Outline each Plasmodium ovale-infected red blood cell.
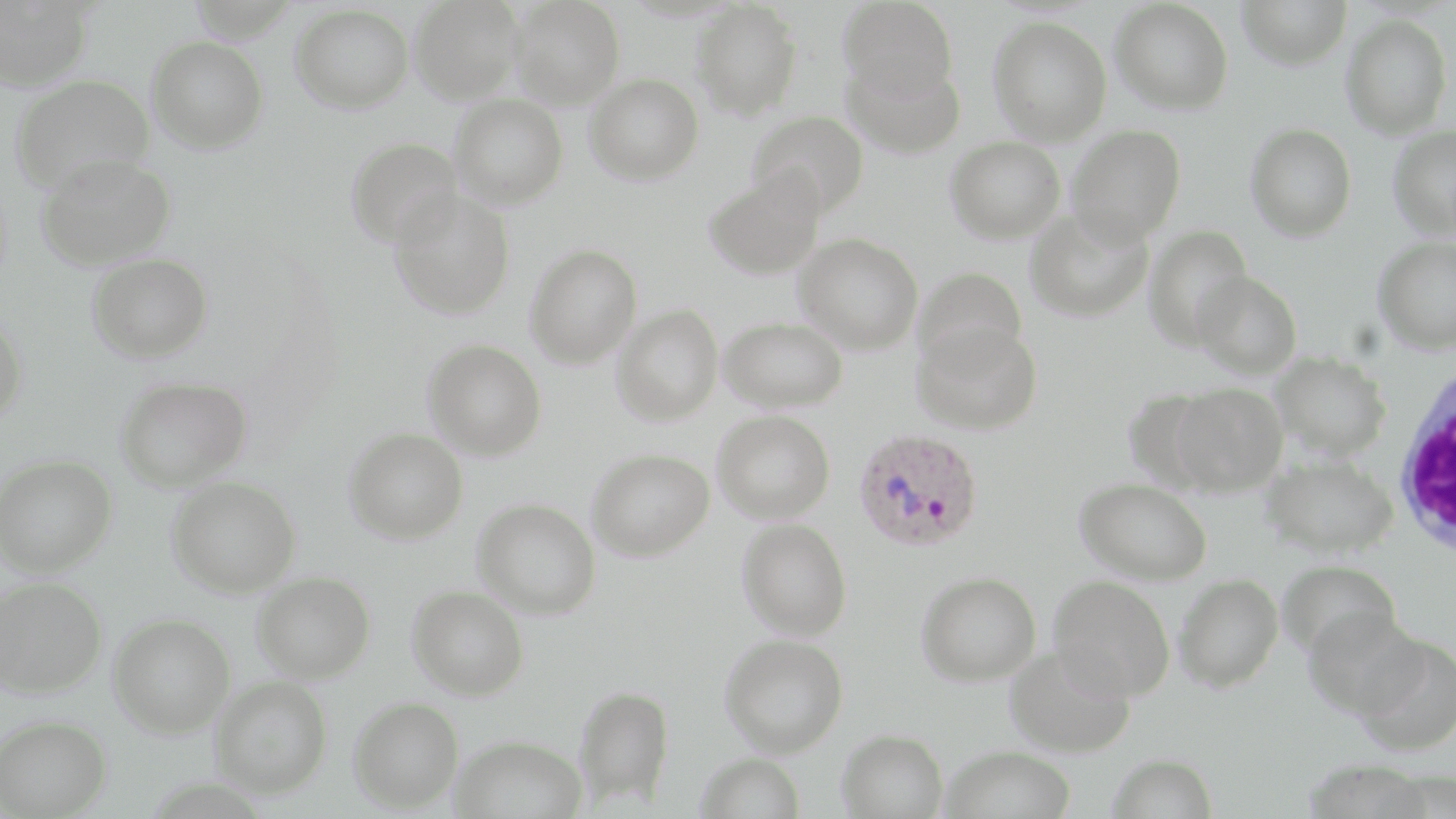
Approximate bounding boxes as (x1,y1)-(x2,y2) corner pairs in pixels.
Plasmodium ovale-infected red blood cells: (854,427)-(984,552).

Uninfected red blood cell locations: (0,0)-(93,91), (409,0)-(523,103), (509,0)-(624,108), (838,0)-(958,102), (1111,0)-(1233,115), (1236,0)-(1352,70), (689,1)-(803,120), (291,4)-(413,114), (1341,14)-(1452,139), (988,17)-(1112,145), (147,36)-(269,153), (844,55)-(966,158), (584,73)-(703,185), (10,74)-(153,193), (450,93)-(568,209), (747,110)-(869,217), (1245,122)-(1357,241), (1066,124)-(1186,246), (1387,126)-(1456,238), (946,136)-(1066,244), (346,137)-(465,248), (36,153)-(175,271), (705,167)-(826,280), (388,190)-(516,320), (1024,207)-(1153,323), (1143,224)-(1253,350), (794,232)-(923,354), (1373,236)-(1456,355), (524,244)-(642,368), (87,253)-(212,364), (914,266)-(1028,371), (1191,270)-(1302,379), (612,304)-(723,426), (0,314)-(28,428), (719,316)-(847,412), (912,320)-(1043,435), (423,339)-(547,460), (1270,351)-(1391,459), (115,375)-(253,491), (1171,383)-(1288,496), (713,410)-(835,524), (343,428)-(468,544), (587,448)-(714,561), (1263,451)-(1398,558), (0,454)-(117,577), (167,476)-(301,598), (1076,477)-(1212,584), (473,498)-(601,619), (737,517)-(852,641), (1278,559)-(1403,661), (252,571)-(375,682), (916,572)-(1041,686), (1174,573)-(1284,692), (1049,575)-(1175,701), (0,576)-(107,699), (407,585)-(529,700), (1302,606)-(1423,719), (108,612)-(235,738), (1352,633)-(1456,756), (720,634)-(848,757), (1005,644)-(1137,757), (210,676)-(333,799), (573,684)-(675,806), (349,696)-(464,812), (1,715)-(112,817), (837,728)-(948,818), (452,734)-(587,819), (941,746)-(1076,819), (695,752)-(806,819), (1107,752)-(1218,818). White blood cell locations: (1393,364)-(1456,565). Slide-level diagnosis: Plasmodium ovale. Image is 1456×819 pixels. One field of a larger specimen. Captured at 1000x magnification. Optical microscopy. May-Grünwald-Giemsa-stained preparation. Thin blood film.